Report the malaria status of this cell.
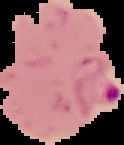
Parasitized.

image size = 124×145 pixels
preparation = thin blood smear
image type = cell region segmented out of the field of view; surrounding area masked to black